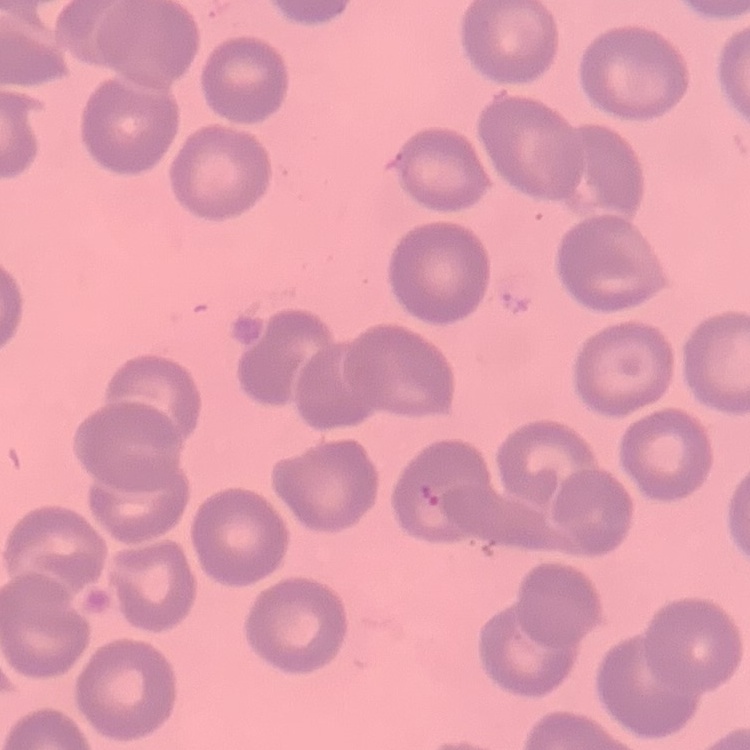
{
  "red_blood_cell_morphology": "no rouleaux formation",
  "stain": "Field's or Giemsa",
  "image_type": "one tile cut from a larger photomicrograph",
  "preparation": "thin blood film"
}